Comment on the morphology of the erythrocytes.
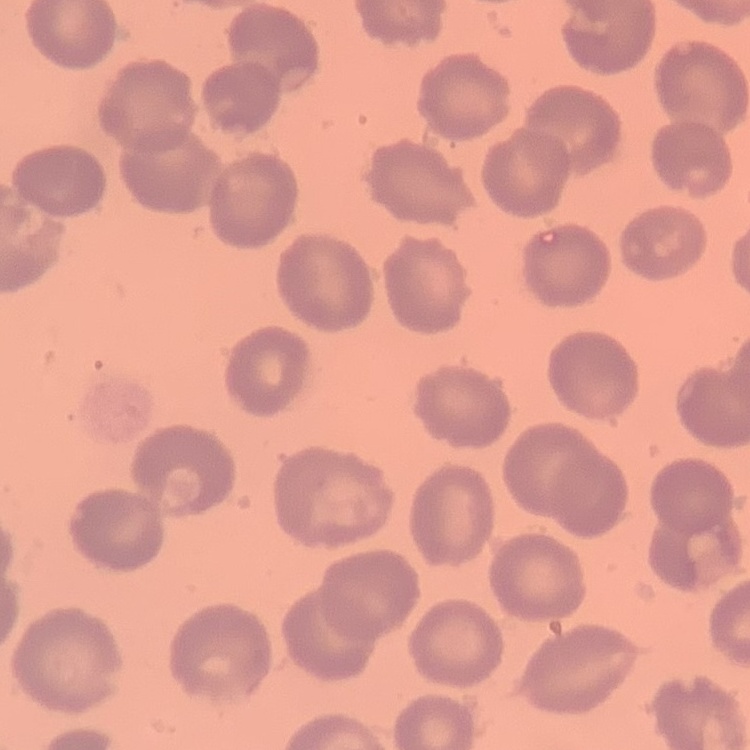
They show no rouleaux formation.

Thin blood smear. Stained with either Field's or Giemsa. Square crop of a larger photomicrograph.